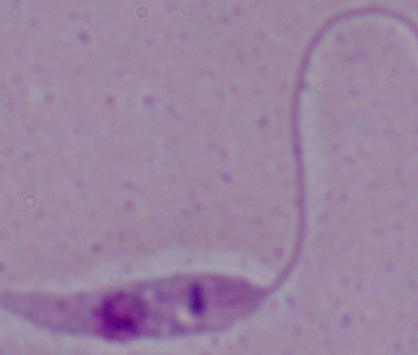

Summary:
  - Magnification: 1000x
  - Identification: Leishmania
  - Modality: micrograph